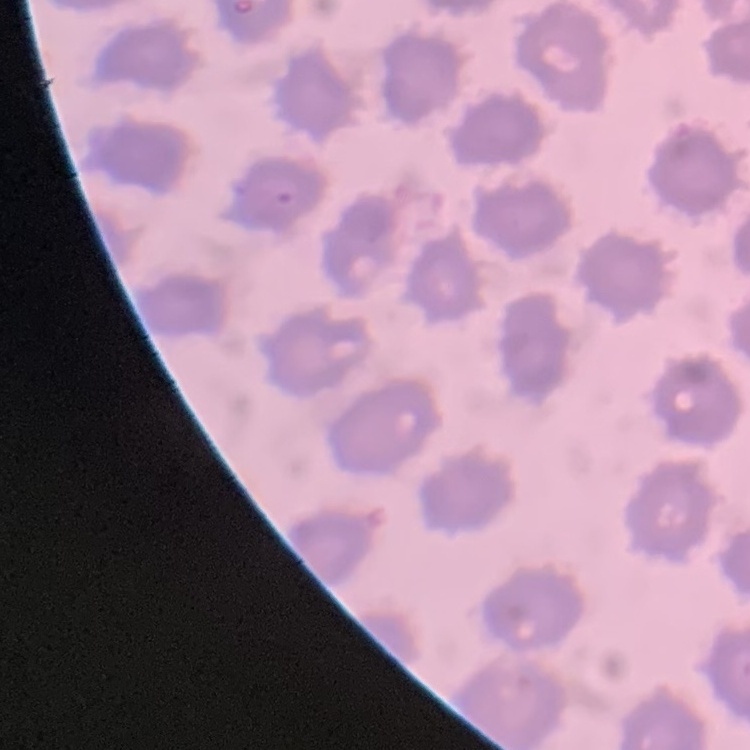

Summary:
  - Red blood cell morphology: no rouleaux formation
  - Preparation: thin blood film
  - Image type: one tile cut from a larger photomicrograph
  - Stain: Field's or Giemsa